Assess this cell for malaria.
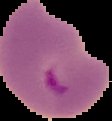

Parasitized.

Summary:
  - Image size: 112×121 pixels
  - Preparation: thin blood smear
  - Image type: cell region segmented out of the field of view; surrounding area masked to black